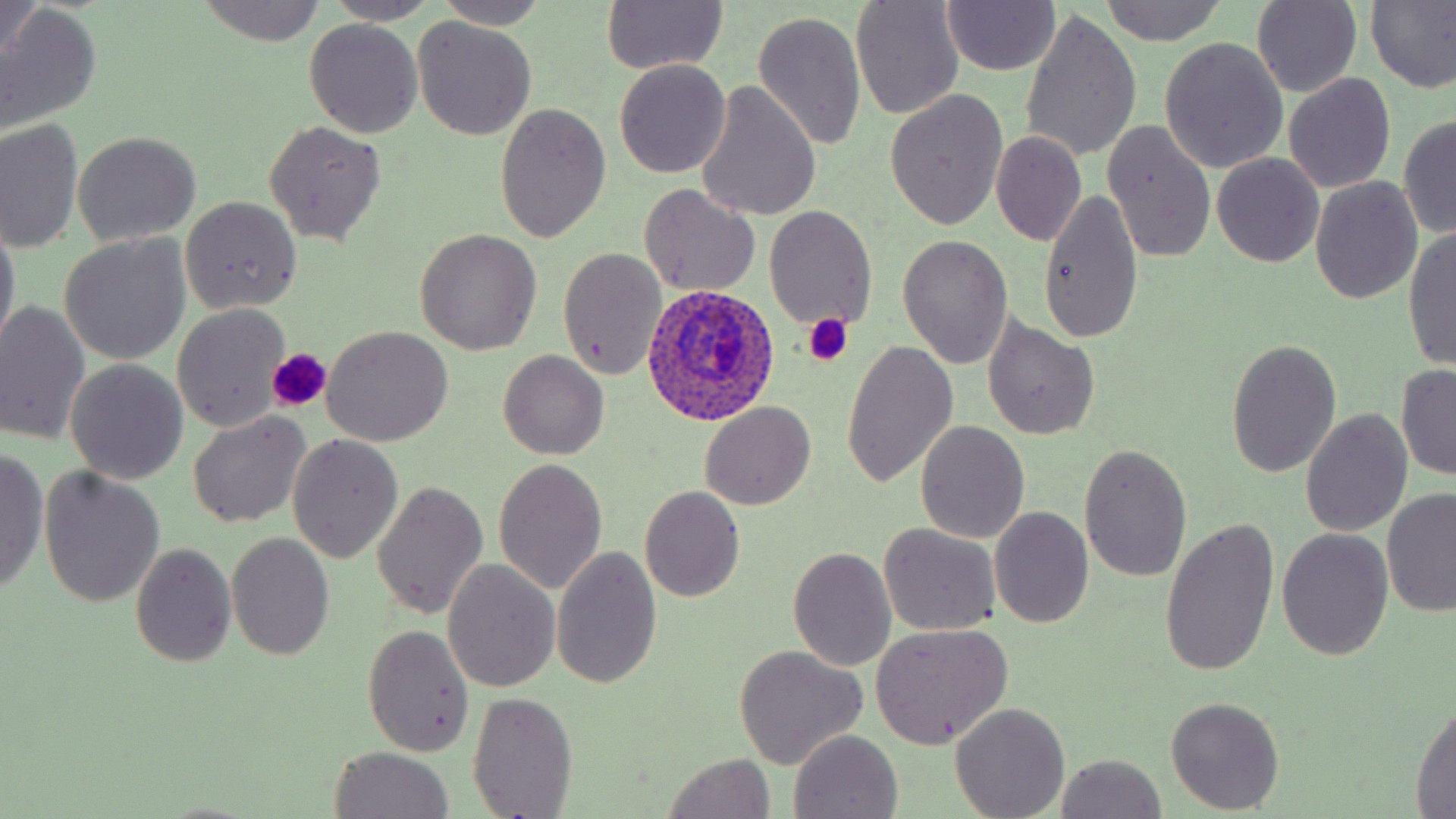
Approximate bounding boxes as [x1, y1, x2, y2] in pixels. Platelet locations: [801, 313, 853, 365], [267, 349, 330, 412]. Uninfected red blood cell locations: [2, 0, 44, 65], [197, 0, 329, 45], [324, 0, 439, 24], [435, 0, 546, 31], [943, 0, 1060, 76], [1101, 0, 1227, 44], [1366, 0, 1456, 93], [601, 1, 729, 75], [850, 2, 965, 119], [1252, 2, 1361, 96], [1, 4, 102, 131], [752, 10, 867, 150], [1021, 11, 1141, 164], [413, 16, 538, 141], [305, 20, 425, 138], [1160, 38, 1288, 173], [614, 59, 732, 179], [1283, 73, 1396, 194], [693, 81, 821, 222], [885, 92, 1008, 230], [494, 101, 612, 242], [1398, 116, 1456, 240], [0, 120, 84, 255], [264, 121, 386, 245], [1104, 123, 1217, 263], [72, 132, 202, 245], [993, 132, 1086, 244], [1212, 153, 1324, 267], [1310, 177, 1423, 304], [638, 184, 761, 297], [1037, 187, 1144, 345], [180, 196, 302, 313], [764, 206, 878, 331], [0, 220, 20, 353], [1404, 225, 1456, 372], [415, 227, 542, 354], [59, 234, 191, 364], [896, 234, 1013, 371], [559, 248, 666, 381], [0, 301, 92, 446], [172, 304, 290, 430], [982, 316, 1101, 439], [324, 326, 453, 445], [1225, 338, 1342, 477], [841, 340, 958, 490], [499, 350, 610, 459], [66, 359, 188, 483], [1396, 363, 1456, 480], [700, 402, 815, 508], [1301, 410, 1413, 537], [187, 412, 310, 527], [915, 420, 1030, 545], [288, 435, 403, 563], [1078, 444, 1193, 583], [0, 447, 49, 596], [493, 457, 607, 597], [39, 467, 166, 606], [371, 480, 488, 621], [640, 487, 745, 601], [1381, 487, 1456, 620], [990, 505, 1095, 628], [1160, 515, 1280, 678], [878, 522, 1001, 637], [1277, 528, 1393, 661], [226, 532, 334, 659], [131, 543, 237, 667], [553, 544, 661, 688], [788, 546, 895, 670], [442, 559, 560, 690], [363, 624, 473, 756], [868, 625, 1011, 751], [734, 645, 869, 771], [468, 691, 580, 819], [1165, 695, 1285, 814], [1411, 703, 1455, 816], [952, 704, 1069, 818], [788, 729, 905, 819], [329, 746, 453, 819], [661, 753, 775, 818], [1054, 754, 1167, 819]. Plasmodium ovale-infected red blood cell locations: [642, 284, 781, 426]. Slide-level diagnosis: Plasmodium ovale. Image is 1456×819 pixels. 1000x magnification. Light microscopy. May-Grünwald-Giemsa stain. Thin blood film. Single field of view.